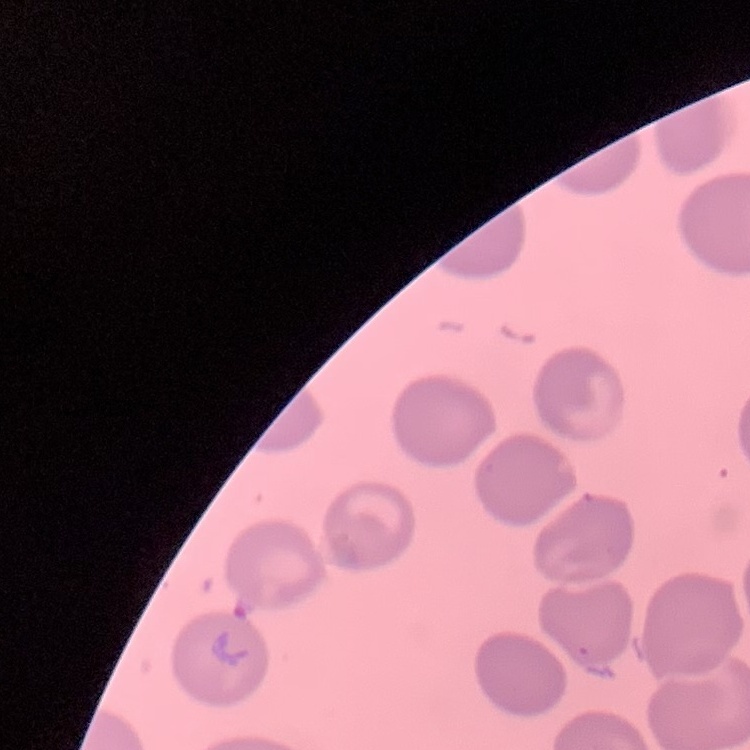
Summary:
  - Red blood cell morphology: no rouleaux formation
  - Image type: square crop of a larger photomicrograph
  - Stain: Field's or Giemsa
  - Preparation: thin blood film